Report the malaria status of this cell.
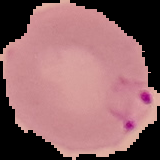
It is parasitized.

preparation = thin blood smear
image type = segmented cell region with the area outside set to black
image size = 160×160 pixels